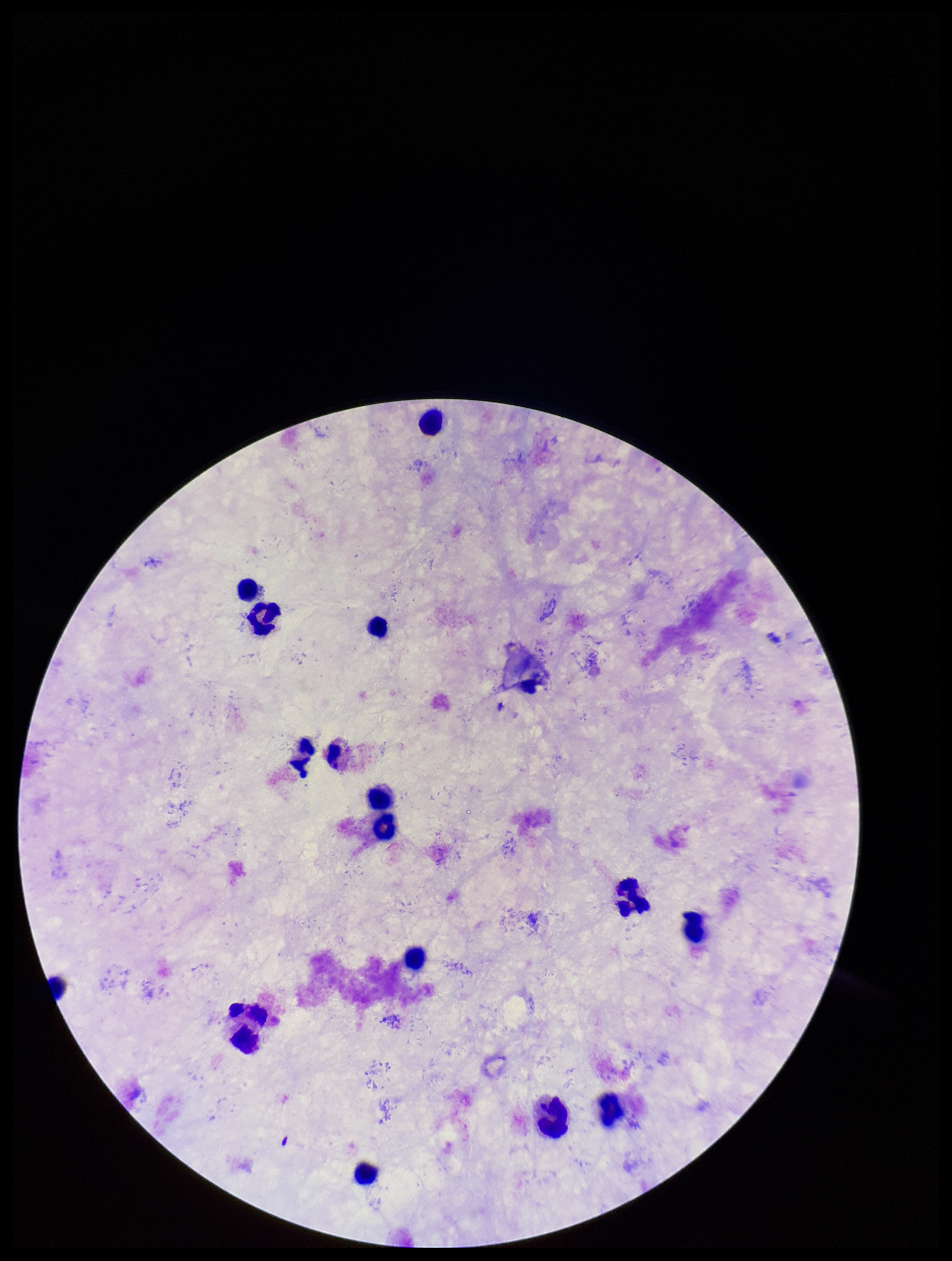 Stained with Giemsa. Preparation: thick blood smear. Photographed through the microscope eyepiece with a smartphone camera. Single field of view. Patient malaria status: negative. Image is 952×1261 pixels. Plasmodium parasites: none detected. Parasite count: 0. Leukocyte count: 15.